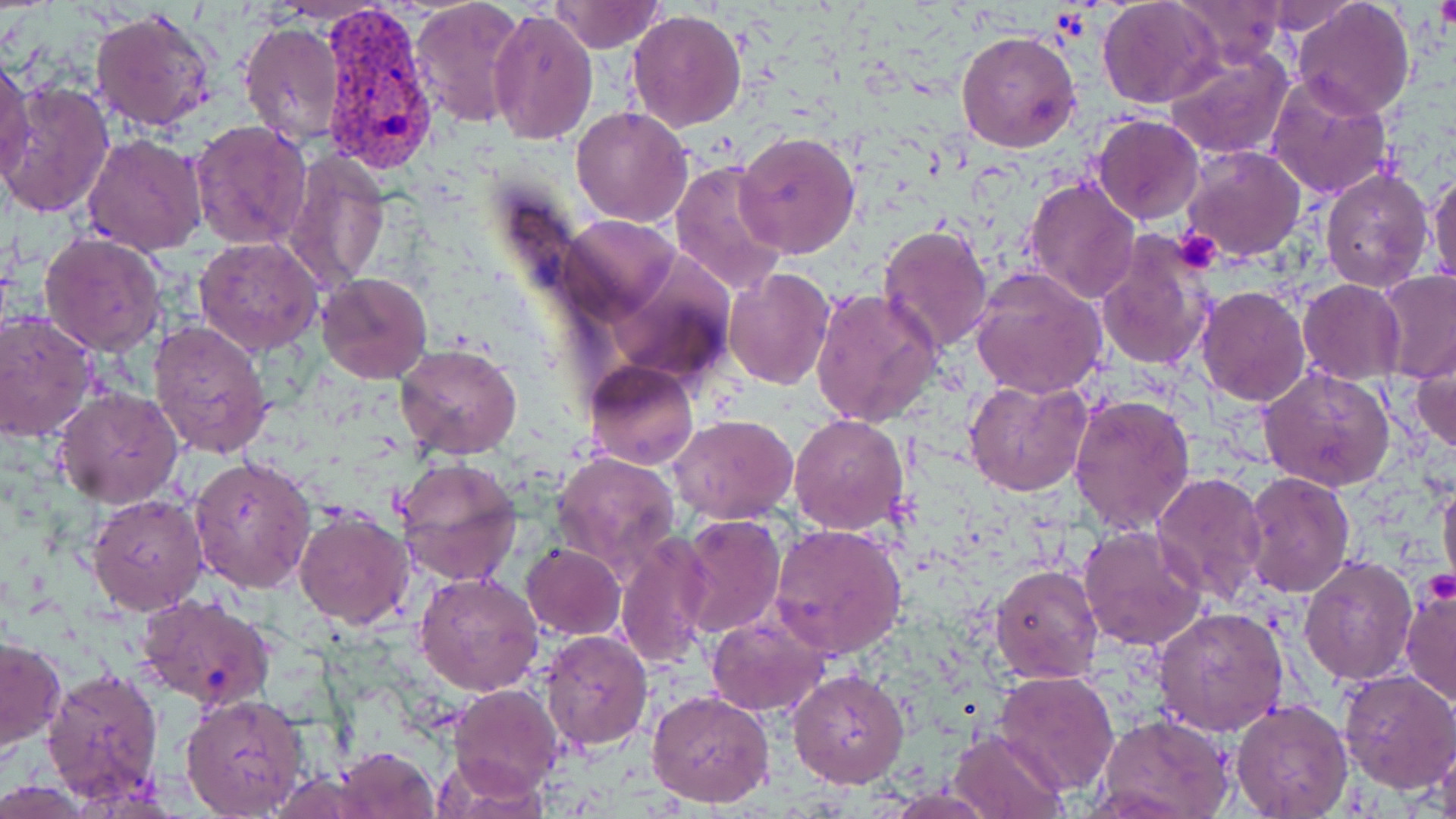
Approximate bounding boxes as (x1,y1)-(x2,y2) corner pairs in pixels. Plasmodium vivax-infected red blood cell locations: (319,9)-(438,174). Uninfected red blood cell locations: (409,0)-(527,127), (549,0)-(666,53), (1097,0)-(1223,109), (1171,0)-(1288,67), (1292,0)-(1416,119), (1257,1)-(1359,35), (486,6)-(597,144), (90,7)-(218,133), (627,9)-(745,132), (236,18)-(345,148), (955,30)-(1081,153), (1164,45)-(1295,159), (0,57)-(36,188), (1266,74)-(1396,201), (1,79)-(115,218), (572,105)-(693,228), (1090,115)-(1205,224), (188,119)-(312,251), (733,131)-(861,260), (81,132)-(208,256), (1181,145)-(1307,262), (281,151)-(393,292), (668,159)-(786,291), (1428,167)-(1456,289), (1320,168)-(1434,294), (1023,177)-(1140,303), (558,213)-(683,324), (878,222)-(994,353), (40,232)-(167,355), (1095,233)-(1215,372), (194,236)-(324,355), (722,267)-(834,390), (969,267)-(1109,400), (1374,269)-(1456,383), (317,272)-(433,383), (1298,279)-(1405,384), (1194,285)-(1311,406), (811,286)-(943,428), (0,311)-(98,442), (149,320)-(274,459), (395,343)-(524,460), (1409,343)-(1456,457), (582,360)-(699,470), (1258,364)-(1397,492), (965,377)-(1093,495), (53,388)-(185,510), (1069,392)-(1197,535), (670,414)-(799,524), (789,414)-(909,533), (552,450)-(681,577), (187,456)-(315,596), (392,456)-(523,585), (1151,472)-(1270,606), (1243,472)-(1356,597), (1438,473)-(1456,600), (86,492)-(207,615), (292,507)-(416,629), (677,514)-(786,637), (770,523)-(906,658), (1077,525)-(1206,651), (614,530)-(711,672), (520,543)-(625,639), (1299,554)-(1418,685), (992,562)-(1103,683), (415,572)-(545,696), (1400,576)-(1456,708), (136,595)-(277,713), (1154,605)-(1289,738), (705,616)-(830,717), (539,630)-(652,751), (0,636)-(65,753), (42,667)-(165,801), (789,668)-(909,787), (993,670)-(1120,795), (1337,670)-(1456,793), (450,685)-(562,796), (647,688)-(775,807), (178,692)-(311,818), (1230,700)-(1352,818), (1097,715)-(1235,819), (947,728)-(1069,818), (1426,733)-(1454,817), (332,746)-(441,819), (433,752)-(552,817). Platelet locations: (1435,0)-(1456,35), (1171,227)-(1223,272). Slide-level diagnosis: Plasmodium vivax. May-Grünwald-Giemsa-stained preparation. One field of a larger specimen. Image is 1456×819 pixels. Captured at 1000x magnification. Thin blood smear. Light microscopy.